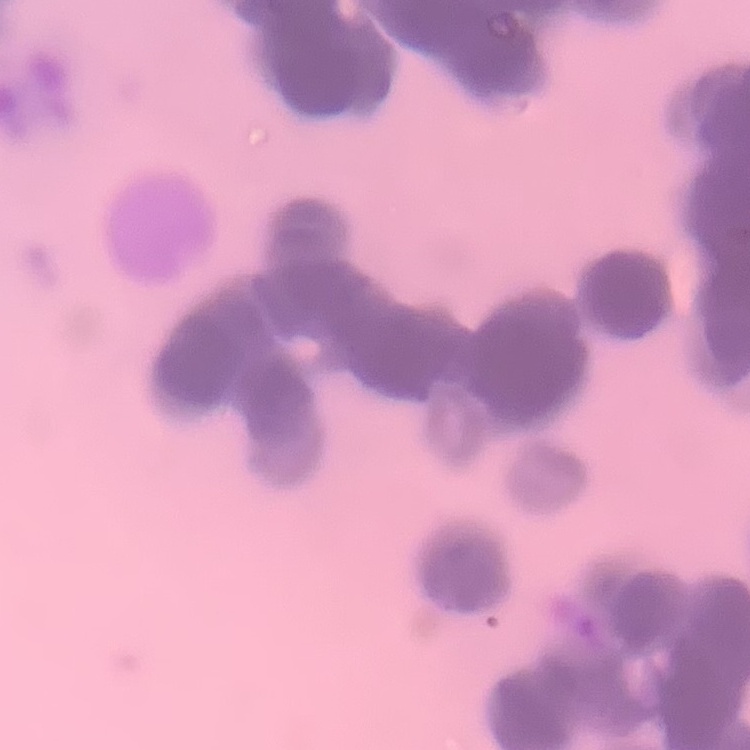

The erythrocytes show rouleaux formation. Thin blood film. Square crop of a larger photomicrograph. Stained with either Field's or Giemsa.